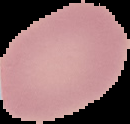 Cell region segmented out of the field of view; the surrounding area is masked to black. From a thin blood smear. Image is 130×124 pixels. Result: no malaria parasites detected.